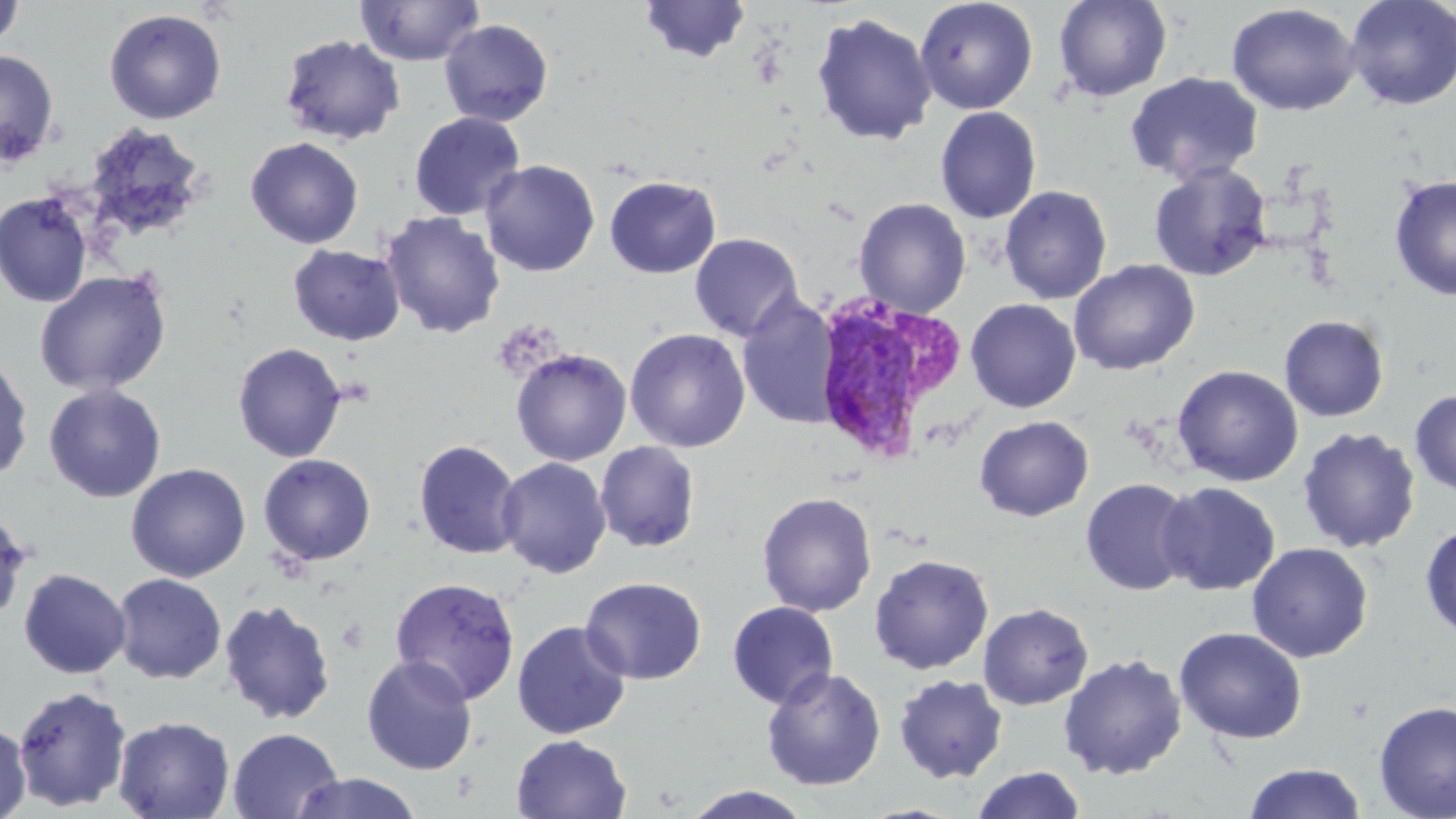

Summary:
  - Coordinate format: approximate bounding boxes as (x1, y1, x2, y2) in pixels
  - Plasmodium vivax-infected red blood cell locations: (809, 295, 964, 465)
  - Uninfected red blood cell locations: (639, 0, 752, 63), (915, 0, 1038, 115), (1053, 0, 1173, 102), (1344, 0, 1456, 110), (0, 1, 24, 51), (355, 1, 485, 67), (1225, 3, 1361, 117), (104, 8, 227, 124), (811, 13, 937, 146), (439, 19, 554, 127), (279, 34, 405, 145), (0, 49, 59, 167), (1125, 71, 1264, 185), (935, 106, 1042, 224), (408, 111, 526, 221), (82, 122, 209, 245), (245, 137, 364, 249), (480, 159, 600, 277), (1149, 162, 1272, 281), (604, 175, 721, 278), (1389, 175, 1456, 301), (999, 185, 1112, 304), (0, 192, 94, 308), (854, 197, 972, 318), (381, 211, 506, 339), (689, 233, 803, 342), (287, 243, 406, 346), (1069, 259, 1199, 376), (34, 270, 172, 396), (736, 292, 841, 430), (966, 298, 1081, 413), (1279, 315, 1389, 421), (625, 327, 751, 453), (232, 342, 347, 463), (511, 348, 632, 466), (1, 352, 34, 484), (1172, 365, 1304, 486), (44, 383, 166, 502), (1410, 389, 1456, 495), (974, 415, 1094, 522), (1297, 426, 1421, 553), (413, 439, 523, 560), (595, 441, 701, 553), (257, 453, 376, 566), (497, 456, 612, 578), (125, 462, 251, 582), (1080, 477, 1197, 596), (1157, 481, 1280, 596), (757, 491, 877, 617), (0, 507, 31, 625), (1420, 523, 1456, 639), (1246, 542, 1373, 662), (869, 553, 994, 674), (18, 567, 131, 679), (112, 572, 226, 683), (389, 576, 521, 704), (580, 576, 707, 685), (219, 598, 336, 726), (727, 600, 839, 709), (978, 602, 1094, 710), (511, 620, 631, 740), (1174, 626, 1307, 743), (1058, 653, 1187, 780), (361, 655, 478, 775), (761, 667, 886, 790), (893, 674, 1009, 783), (13, 684, 131, 811), (1374, 700, 1456, 819), (112, 715, 235, 818), (0, 720, 31, 819), (228, 727, 343, 818), (511, 734, 632, 819), (1243, 763, 1367, 819), (971, 766, 1087, 819), (289, 772, 423, 818), (682, 785, 814, 819)
  - Slide-level diagnosis: Plasmodium vivax
  - Preparation: thin blood film
  - Modality: optical microscopy
  - Magnification: 1000x
  - Field of view: single
  - Image size: 1456×819 pixels
  - Stain: May-Grünwald-Giemsa